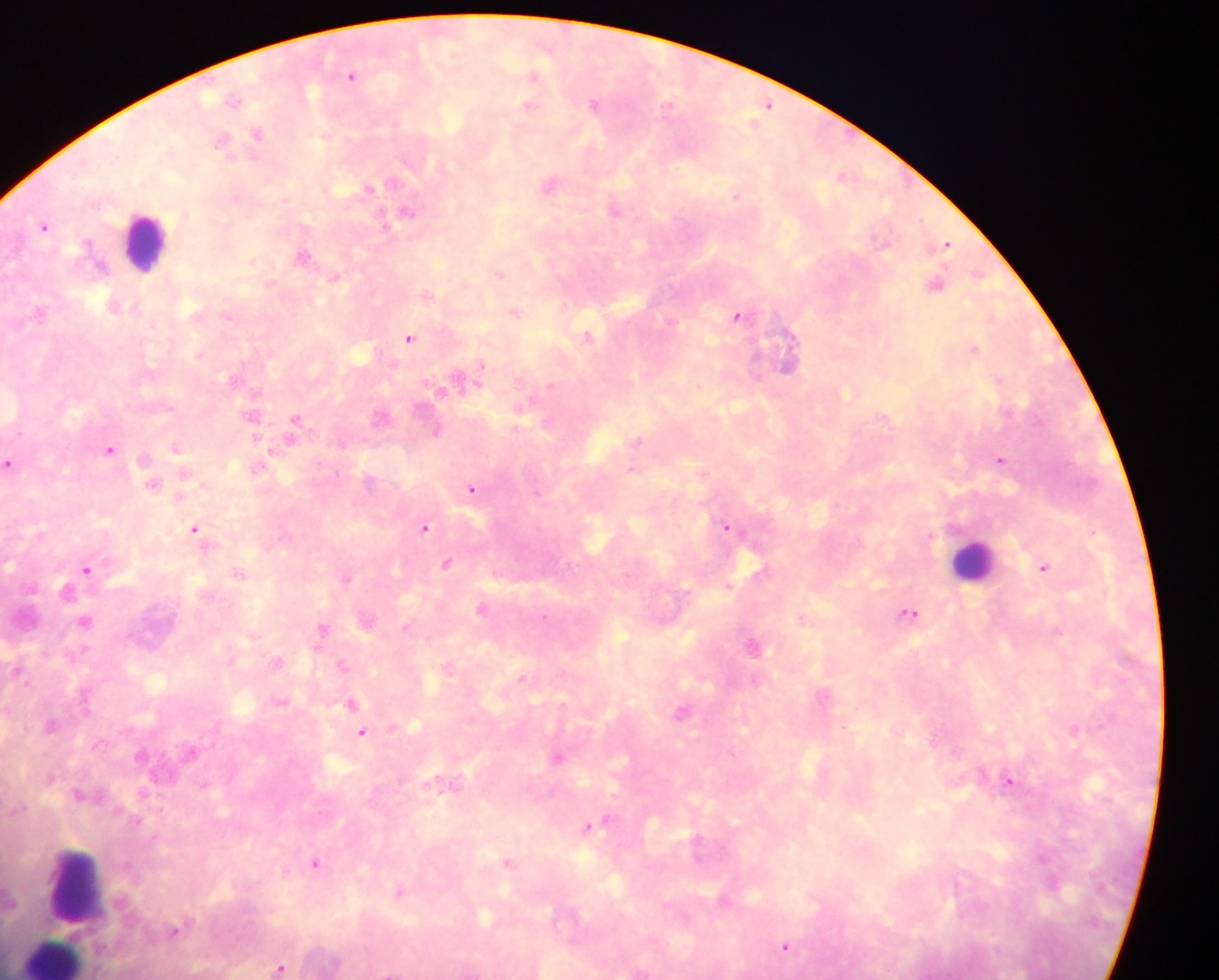

field of view = single
image size = 1219×980 pixels
country = Ghana
preparation = thick blood film
malaria parasite locations = approximate centers as {x, y} in pixels: {353, 72}, {533, 75}, {236, 99}, {594, 102}, {527, 104}, {256, 131}, {221, 137}, {231, 157}, {372, 187}, {737, 194}, {409, 209}, {304, 255}, {500, 273}, {336, 276}, {515, 311}, {740, 313}, {227, 315}, {991, 318}, {589, 335}, {409, 336}, {976, 346}, {482, 364}, {440, 390}, {297, 418}, {437, 431}, {257, 436}, {639, 440}, {177, 447}, {111, 448}, {1001, 460}, {9, 464}, {634, 467}, {704, 472}, {185, 473}, {154, 482}, {471, 487}, {180, 493}, {726, 524}, {425, 527}, {195, 529}, {446, 562}, {1045, 567}, {87, 569}, {240, 574}, {345, 578}, {729, 583}, {910, 611}, {544, 616}, {803, 617}, {86, 621}, {323, 627}, {1057, 630}, {753, 642}, {277, 661}, {341, 665}, {563, 670}, {524, 676}, {353, 701}, {52, 725}, {1075, 727}, {362, 732}, {558, 756}, {1011, 781}, {609, 818}, {588, 826}, {1041, 859}, {316, 861}, {510, 862}, {786, 944}, {279, 966}
capture = mobile-phone photograph through a microscope